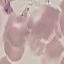
malaria status = uninfected
image type = cell patch, automatically extracted from a larger field of view and resized to 64 × 64 pixels
stain = Giemsa
preparation = thin blood film
capture = smartphone camera at the microscope eyepiece